Locate every Plasmodium parasite.
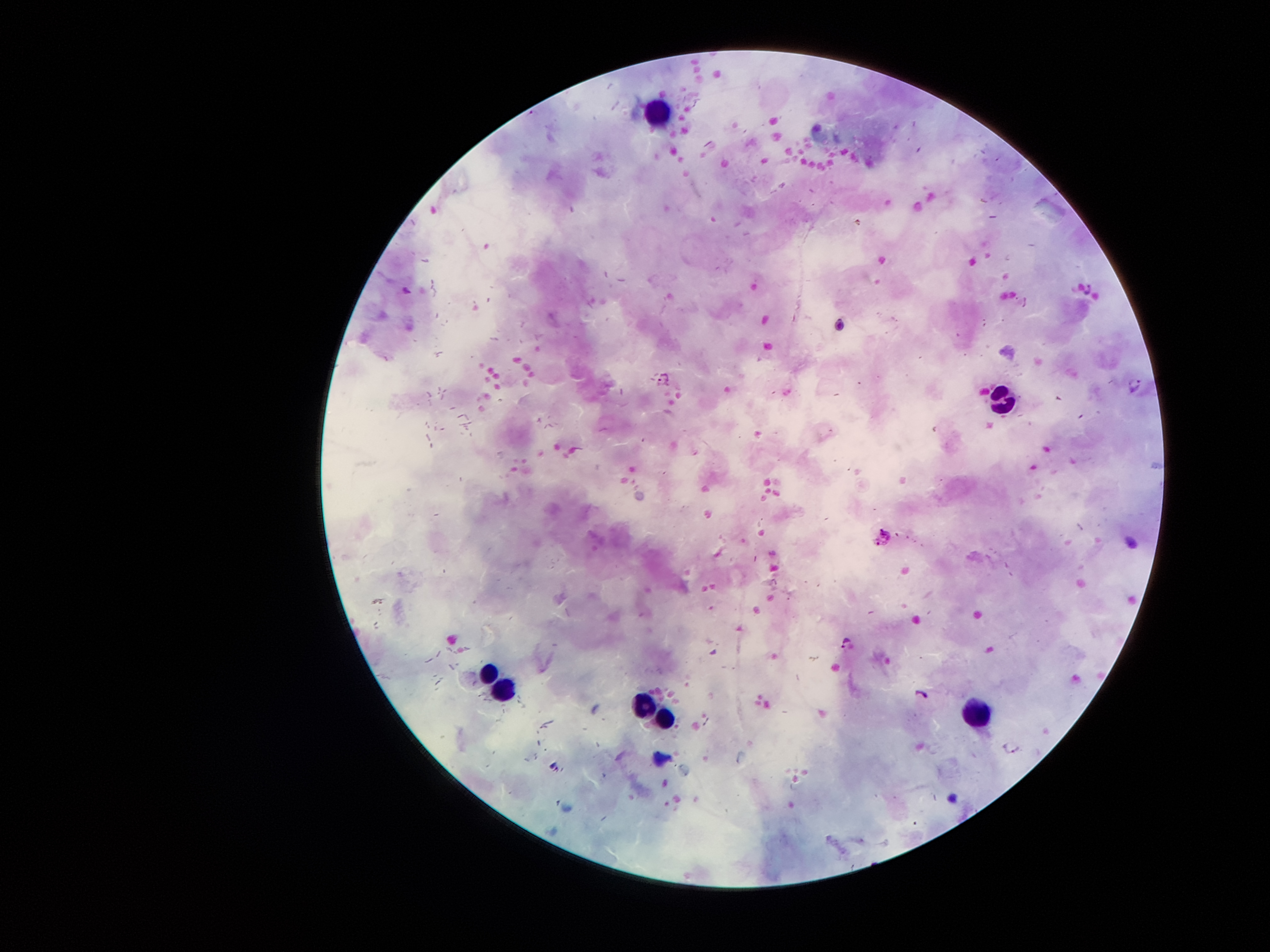
Approximate centers as {x, y} in pixels.
Plasmodium parasites: {532, 112}, {663, 380}, {1136, 383}, {847, 643}, {922, 692}.

Summary:
  - Leukocyte locations: {654, 112}, {999, 401}, {489, 667}, {505, 686}, {644, 705}, {977, 709}, {663, 719}
  - Image size: 1270×952 pixels
  - Capture: smartphone through the microscope eyepiece
  - Patient malaria status: infected with Plasmodium falciparum
  - Preparation: thick blood smear
  - Field of view: one from this slide
  - Magnification: 100x
  - Stain: Giemsa